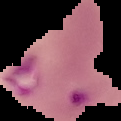
From a thin blood smear. Cell region segmented out of the field of view; the surrounding area is masked to black. Malaria status: parasitized. Image is 121×121 pixels.